Comment on the morphology of the erythrocytes.
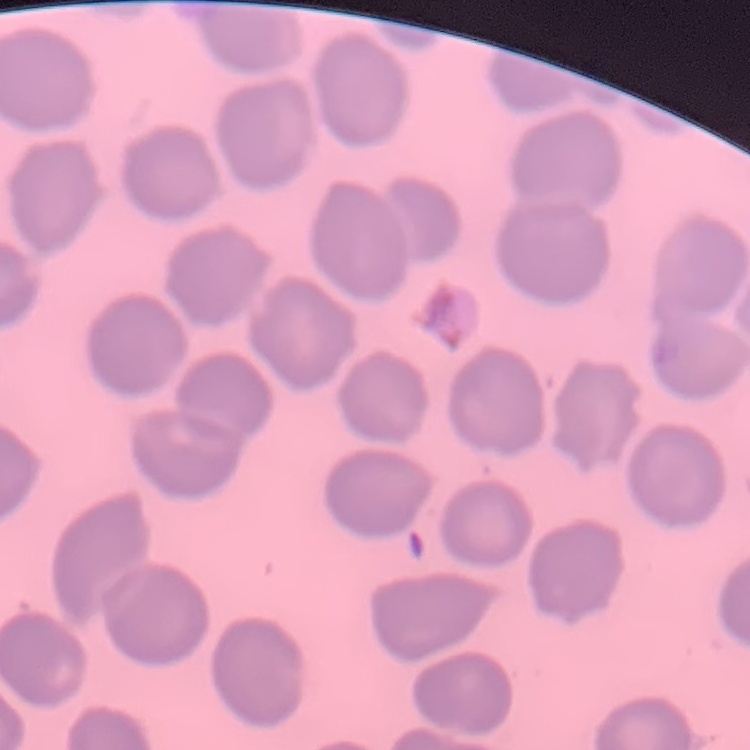

They show no rouleaux formation.

stain: Field's or Giemsa
image_type: square crop of a larger photomicrograph
preparation: thin blood smear